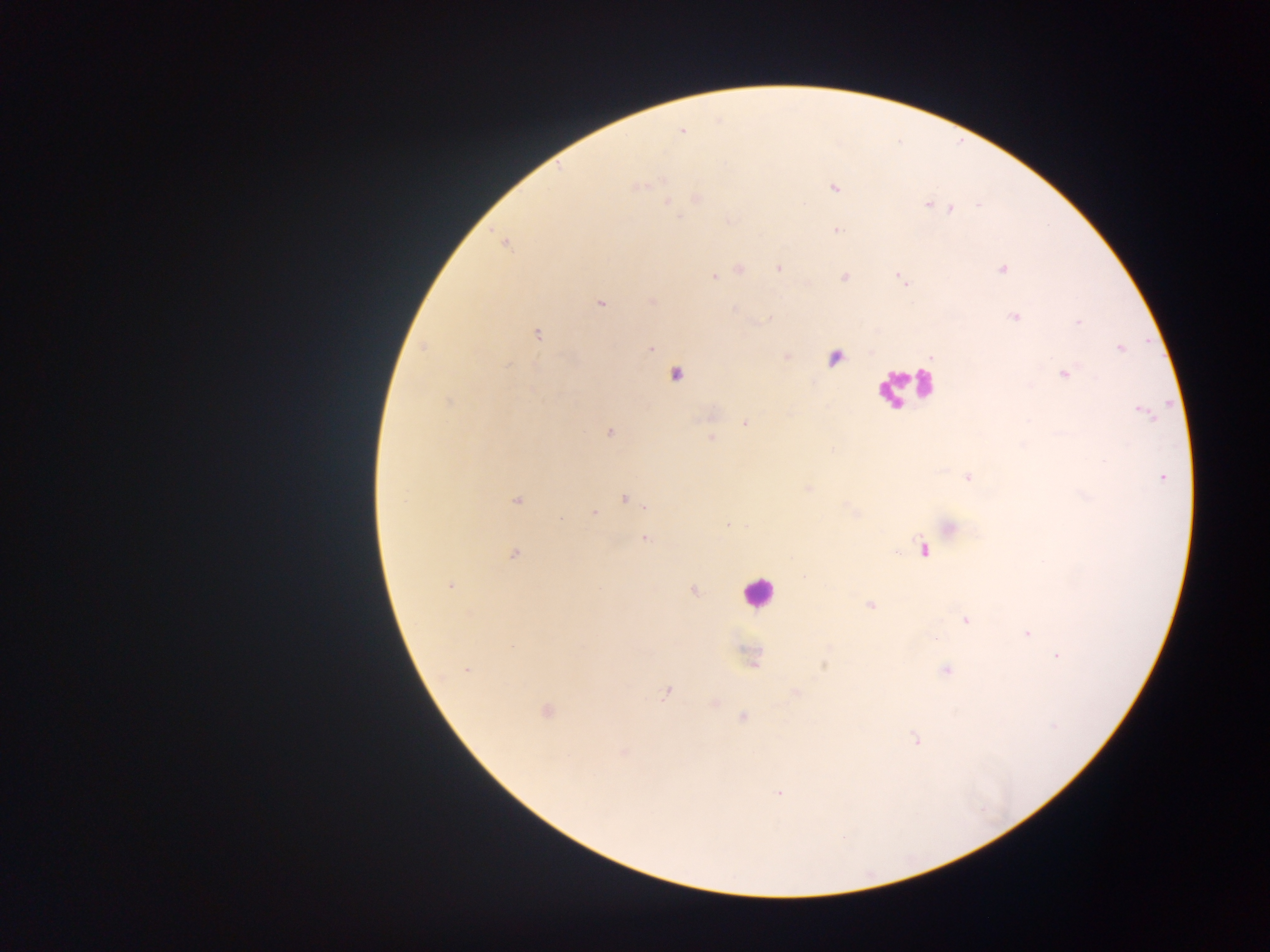
field of view = single
Plasmodium parasite locations = approximate centers as [x, y] in pixels: [682, 131], [637, 185], [834, 188], [696, 198], [667, 202], [928, 204], [950, 209], [837, 231], [503, 241], [780, 267], [1002, 268], [739, 270], [714, 276], [844, 277], [901, 279], [652, 300], [600, 303], [1015, 315], [536, 334], [651, 348], [1121, 348], [786, 356], [834, 357], [1064, 373], [674, 375], [448, 401], [1140, 410], [745, 423], [609, 432], [711, 438], [968, 477], [1162, 477], [807, 487], [625, 498], [517, 500], [593, 513], [728, 525], [949, 527], [645, 537], [924, 549], [514, 553], [450, 584], [693, 590], [870, 605], [965, 620], [1027, 633], [1058, 655], [752, 657], [823, 662], [467, 670], [946, 670], [667, 691], [795, 693], [714, 703], [546, 710], [742, 717], [916, 739], [623, 752], [779, 793]
capture = mobile-phone photograph through a microscope
leukocyte locations = approximate centers as [x, y] in pixels: [907, 387], [757, 591]
preparation = thick blood smear
country = Ghana
image size = 1270×952 pixels